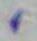
Summary:
  - Modality: micrograph
  - Magnification: 1000x
  - Identification: Toxoplasma gondii